Evaluate for malaria.
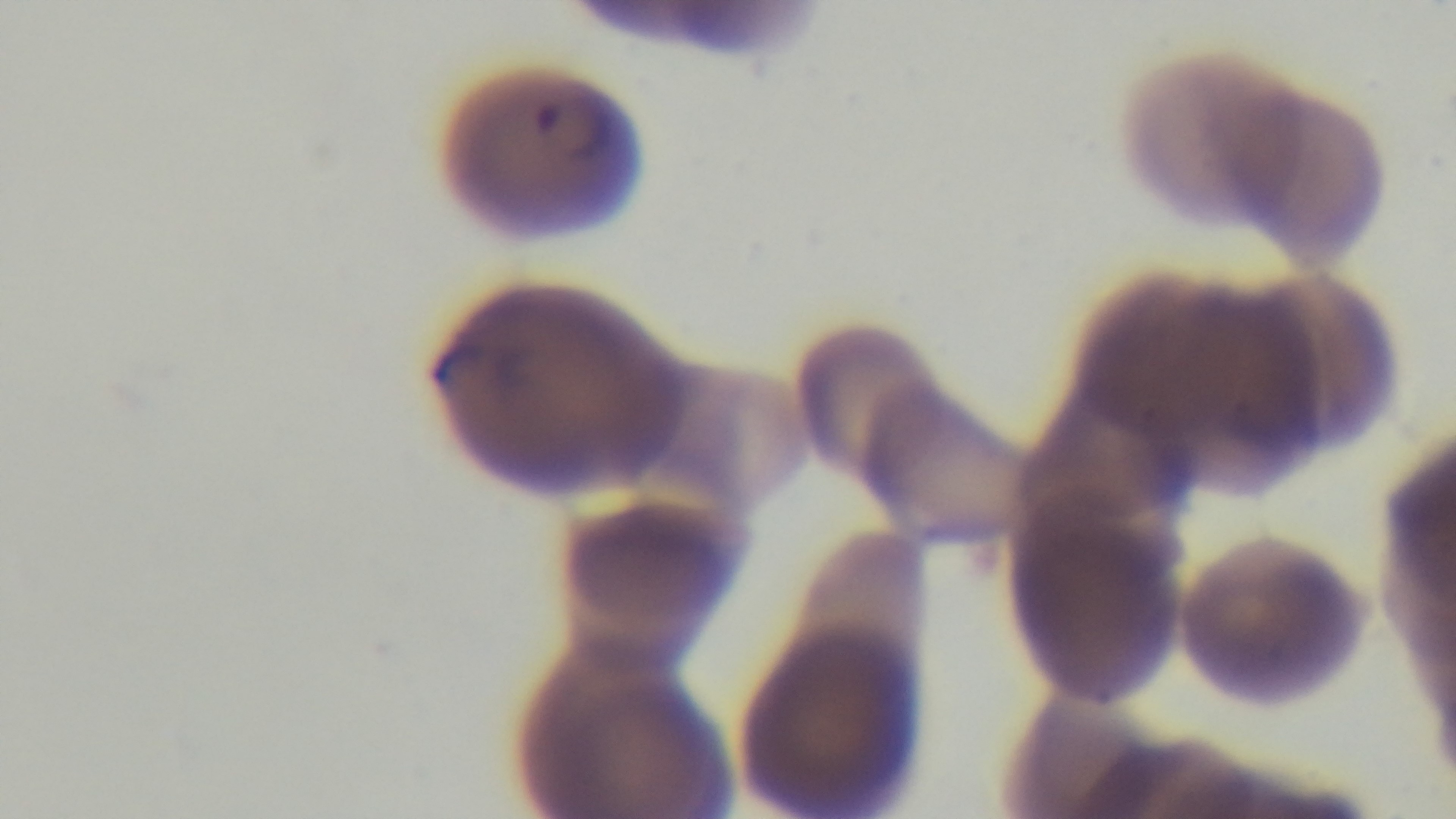

Positive.

Summary:
  - Field of view: single
  - Preparation: thin
  - Capture: mounted 4K digital camera
  - Objective: 100x oil immersion
  - Stain: Giemsa
  - Modality: light microscopy